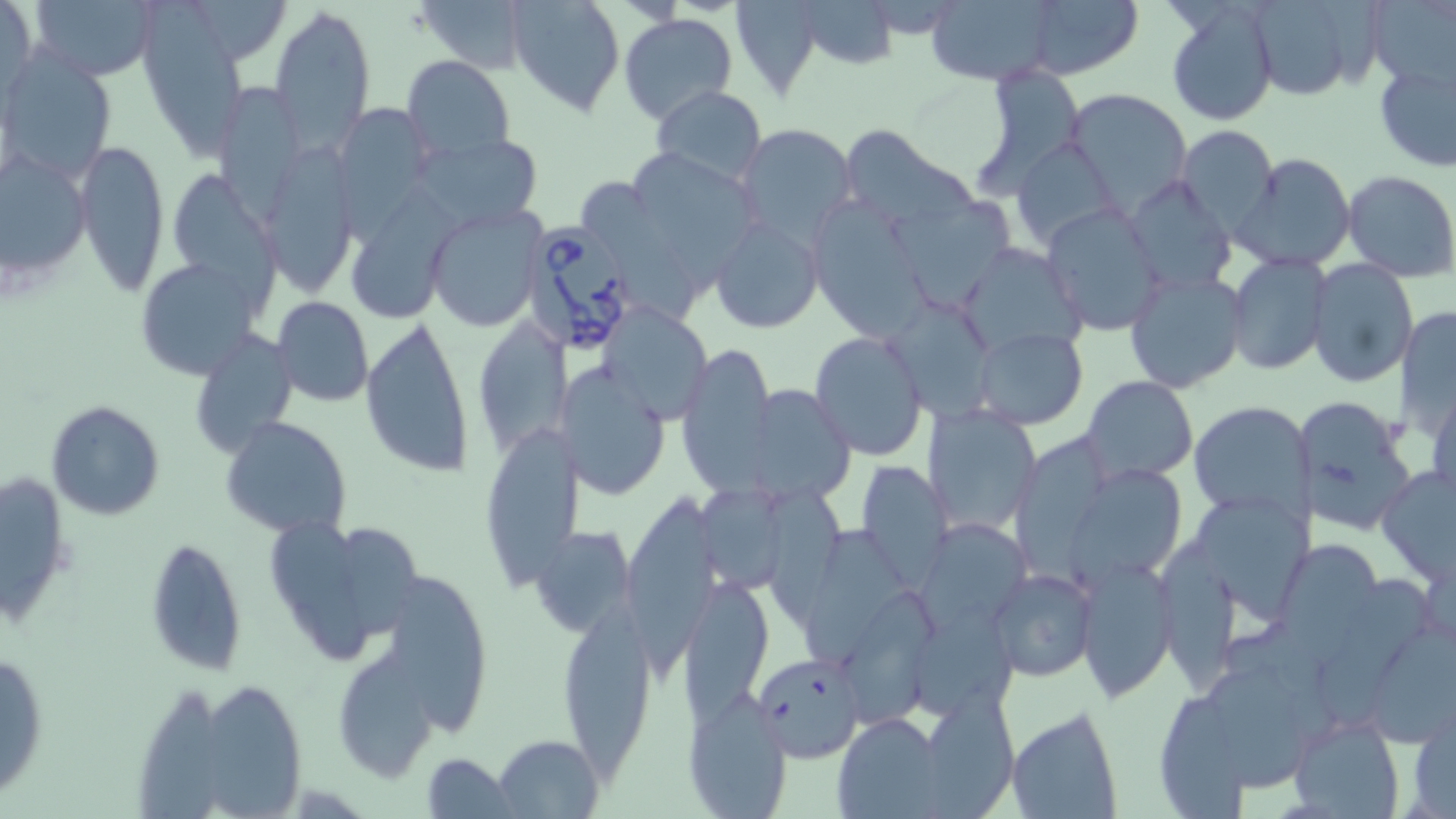
Summary:
  - Coordinate format: approximate bounding boxes as (x1, y1, x2, y2) in pixels
  - Uninfected red blood cell locations: (412, 0, 535, 75), (506, 0, 626, 117), (730, 0, 823, 99), (796, 0, 899, 67), (926, 0, 1065, 86), (1024, 0, 1142, 80), (1240, 0, 1379, 101), (1368, 0, 1454, 90), (25, 1, 161, 79), (144, 1, 243, 158), (0, 2, 40, 102), (1163, 3, 1279, 127), (268, 5, 375, 144), (619, 14, 738, 126), (3, 51, 117, 183), (403, 56, 515, 165), (1373, 61, 1456, 172), (972, 63, 1088, 196), (212, 83, 310, 218), (651, 85, 767, 185), (1064, 88, 1196, 209), (336, 104, 433, 223), (735, 123, 857, 245), (836, 124, 968, 229), (1174, 124, 1279, 235), (413, 130, 546, 233), (1011, 137, 1121, 253), (74, 139, 169, 298), (630, 143, 758, 294), (260, 144, 358, 295), (0, 149, 90, 282), (1233, 153, 1357, 272), (1342, 171, 1456, 280), (1126, 175, 1237, 295), (172, 179, 278, 311), (584, 182, 694, 328), (355, 194, 463, 324), (888, 196, 1027, 321), (806, 197, 935, 340), (1041, 203, 1163, 334), (427, 205, 549, 330), (711, 214, 824, 333), (958, 242, 1087, 359), (1227, 252, 1330, 376), (136, 257, 262, 376), (1307, 259, 1417, 389), (1123, 268, 1249, 393), (272, 296, 375, 406), (601, 301, 714, 423), (888, 301, 993, 425), (1396, 306, 1456, 438), (472, 314, 566, 462), (360, 315, 474, 482), (972, 326, 1089, 429), (188, 329, 299, 459), (809, 330, 928, 461), (677, 342, 777, 493), (562, 360, 672, 500), (1081, 376, 1197, 483), (753, 383, 853, 505), (1427, 384, 1455, 503), (1292, 394, 1418, 533), (1189, 399, 1315, 521), (45, 400, 164, 521), (925, 402, 1045, 536), (220, 416, 352, 538), (481, 422, 582, 595), (1015, 433, 1120, 581), (856, 462, 953, 585), (1, 465, 72, 625), (1377, 465, 1454, 582), (1068, 472, 1187, 590), (701, 480, 788, 589), (632, 488, 722, 682), (766, 491, 848, 623), (1186, 491, 1314, 617), (920, 520, 1029, 631), (275, 521, 374, 664), (341, 524, 423, 638), (534, 525, 634, 637), (795, 527, 917, 672), (1157, 534, 1235, 691), (144, 537, 248, 675), (1283, 541, 1377, 670), (1074, 556, 1177, 700), (989, 567, 1097, 682), (1320, 574, 1438, 727), (678, 577, 774, 718), (396, 578, 487, 735), (842, 587, 939, 724), (913, 605, 1016, 720), (559, 610, 654, 768), (1364, 622, 1455, 744), (0, 649, 49, 801), (749, 650, 866, 766), (332, 652, 442, 784), (1210, 669, 1335, 790), (135, 684, 221, 819), (208, 689, 301, 819), (916, 690, 1021, 815), (1156, 695, 1248, 819), (684, 696, 789, 818), (1004, 705, 1124, 819), (1409, 711, 1454, 819), (1288, 712, 1405, 819), (833, 714, 945, 817), (494, 735, 604, 819), (423, 754, 516, 818)
  - Babesia divergens-infected red blood cell locations: (519, 217, 646, 356)
  - Slide-level diagnosis: Babesia divergens
  - Magnification: 1000x
  - Image size: 1456×819 pixels
  - Stain: May-Grünwald-Giemsa
  - Field of view: single
  - Modality: optical microscopy
  - Preparation: thin blood smear